Comment on the morphology of the erythrocytes.
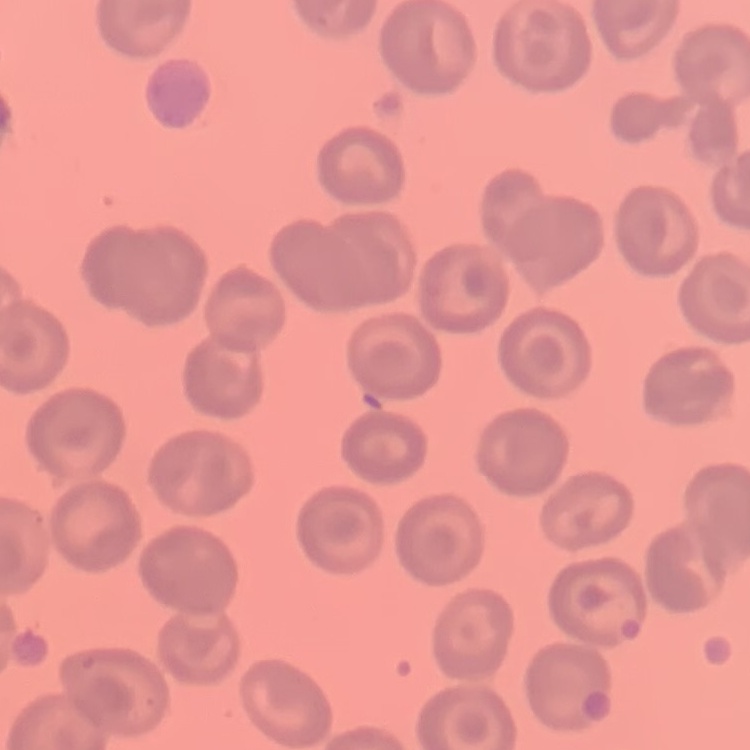

No rouleaux formation.

{
  "stain": "Field's or Giemsa",
  "image_type": "one tile cut from a larger photomicrograph",
  "preparation": "thin blood smear"
}